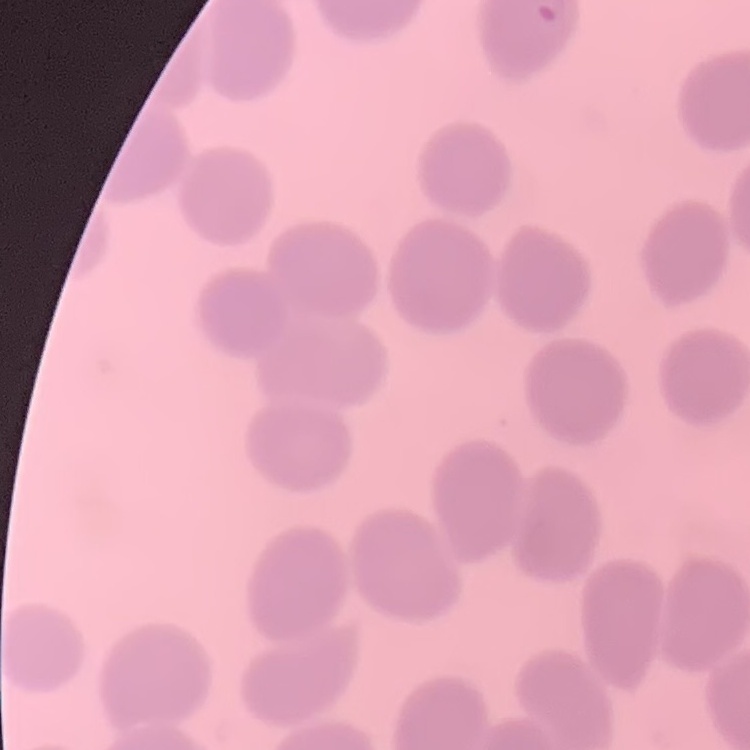 The erythrocytes exhibit no rouleaux formation. One tile cut from a larger photomicrograph. Thin blood smear. Field's or Giemsa stain.